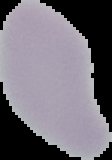
Malaria status: uninfected. Cell region segmented out of the field of view; the surrounding area is masked to black. From a thin blood smear. Image is 112×160 pixels.